Comment on the background quality.
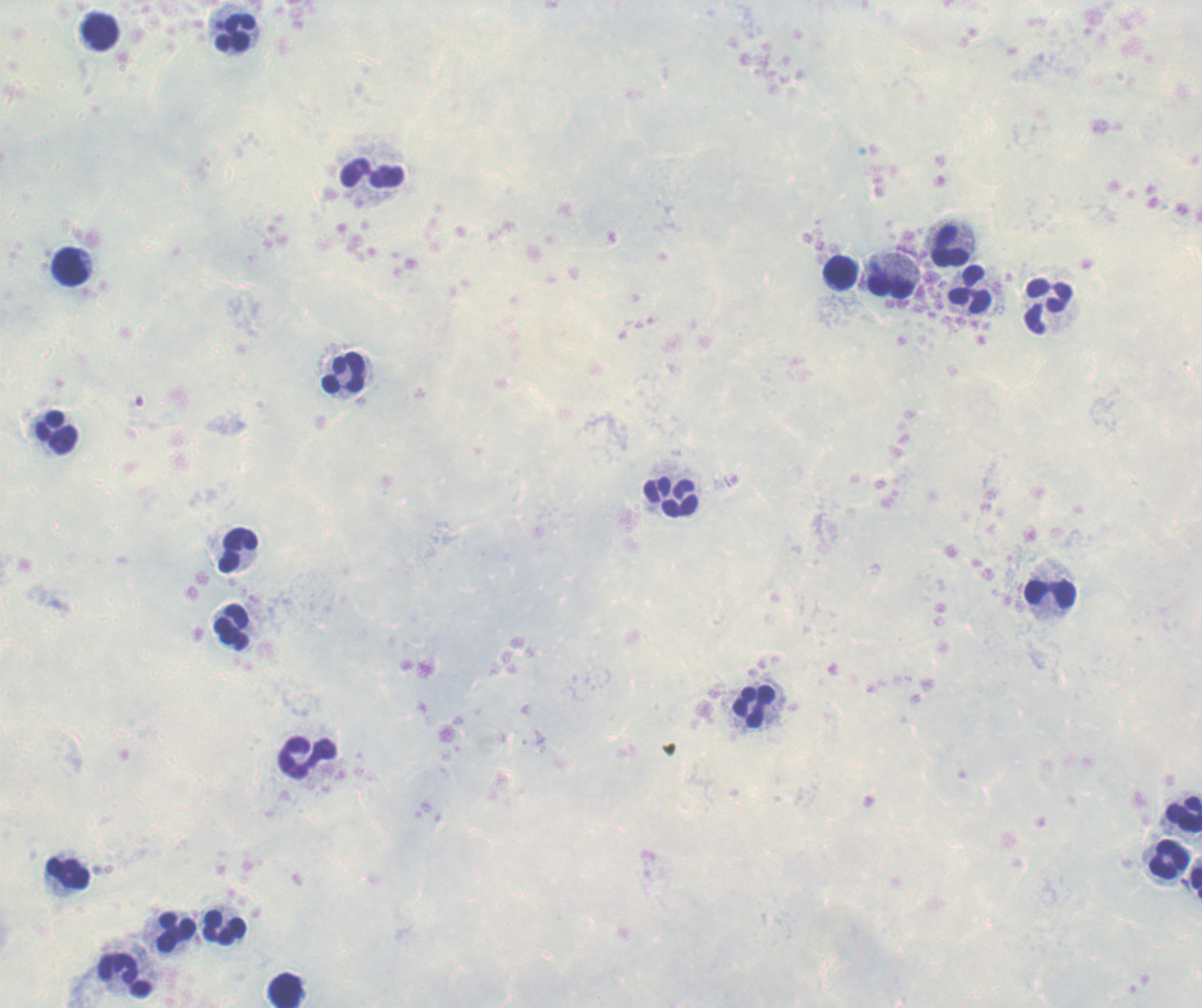

It is poor.

context: previously used in an actual diagnosis
result: no malaria parasites detected
preparation: thick blood film
field_of_view: single
magnification: 100x
leukocyte_locations: 'approximate centers as [x, y] in pixels: [99, 31], [235, 32], [373, 172], [949, 247], [69, 266], [841, 273], [891, 285], [970, 289], [1048, 305], [343, 374], [56, 432], [671, 497], [239, 550], [1050, 593], [231, 627], [753, 706], [307, 756], [1184, 813], [1169, 858], [68, 873], [1197, 883], [225, 927], [177, 932], [125, 976], [285, 989]'
stain: Romanowsky
image_size: 1202×1008 pixels